Classify this cell by malaria status.
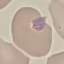

It is uninfected.

Summary:
  - Stain: Giemsa
  - Preparation: thin blood film
  - Capture: smartphone through the microscope eyepiece
  - Image type: automatically extracted cell patch, resized to 64 × 64 pixels